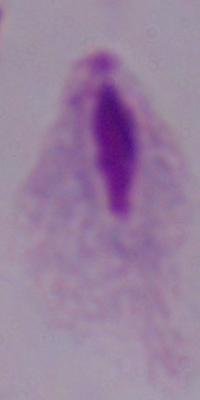

Photomicrograph. Captured at 1000x magnification. A trichomonad is seen.